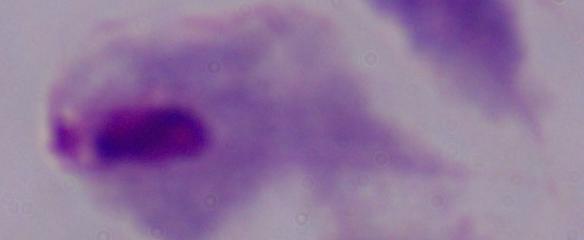

Summary:
  - Identification: trichomonad
  - Modality: photomicrograph
  - Magnification: 1000x